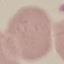 Result: no malaria parasites detected. Photographed with a smartphone camera at the microscope eyepiece. Cell patch, automatically extracted from a larger field of view and resized to 64 × 64 pixels. Thin blood smear. Giemsa stain.